Give the position of every Plasmodium parasite.
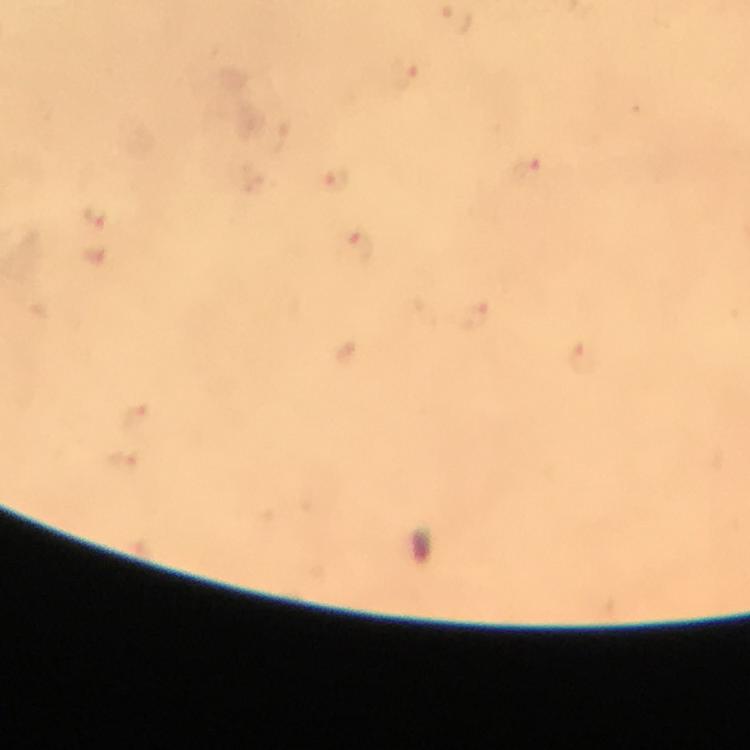
Approximate centers as (x, y) in pixels.
Plasmodium parasites: (337, 178), (361, 245).

Summary:
  - Preparation: thick blood smear
  - Stain: Giemsa
  - Context: from a diagnostic examination for malaria
  - Capture: smartphone mounted on the microscope
  - Image size: 750×750 pixels
  - Magnification: 100x
  - Immersion oil: used
  - Cropped from: a single field of view